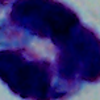

Summary:
  - Modality: photomicrograph
  - Magnification: 1000x
  - Identification: white blood cell